Assess this cell for malaria.
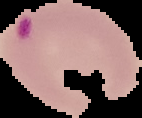
Parasitized.

{
  "preparation": "thin blood film",
  "image_type": "segmented cell region with the area outside set to black",
  "image_size": "142×118 pixels"
}